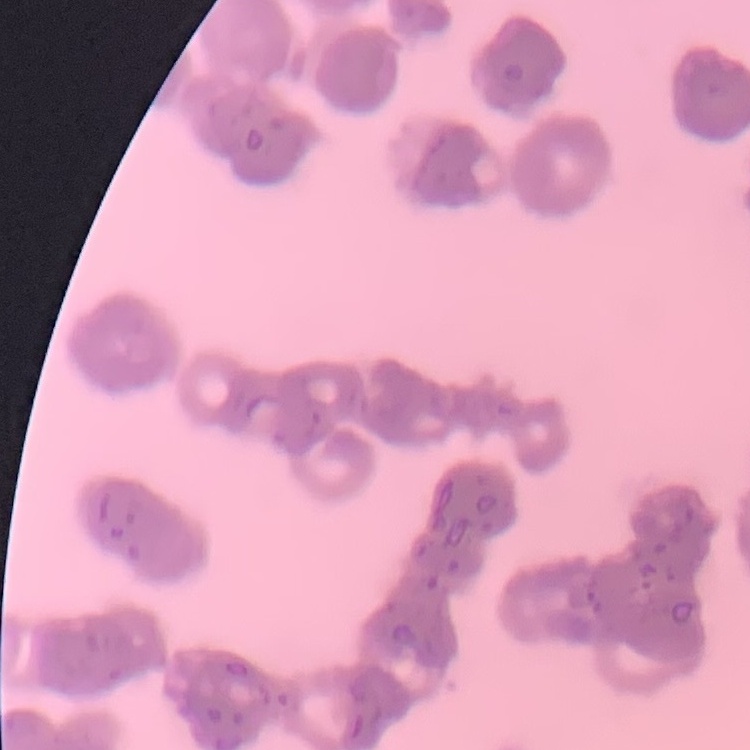

Summary:
  - Red blood cell morphology: rouleaux formation
  - Image type: square crop of a larger photomicrograph
  - Stain: Field's or Giemsa
  - Preparation: thin blood film